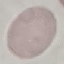
Malaria status: uninfected. Giemsa stain. Automatically extracted cell patch, resized to 64 × 64 pixels. Thin blood smear. Photographed with a smartphone camera at the microscope eyepiece.